Classify this cell by malaria status.
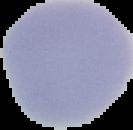
Uninfected.

From a thin blood smear. Cell region segmented out of the field of view; the surrounding area is masked to black. Image is 133×130 pixels.